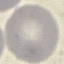
result = negative for malaria parasites
preparation = thin blood smear
capture = smartphone camera at the microscope eyepiece
image type = cell patch, automatically extracted from a larger field of view and resized to 64 × 64 pixels
stain = Giemsa